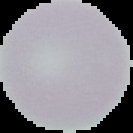
Result: negative for Plasmodium parasites. The area outside the segmented cell region is set to black. Image is 133×133 pixels. From a thin blood film.